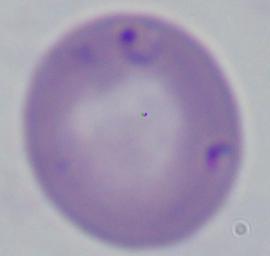 Captured at 1000x magnification. A Babesia parasite is shown. Micrograph.